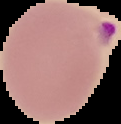

Image is 121×124 pixels. The area outside the segmented cell region is set to black. Malaria status: parasitized. From a thin blood film.